Locate every blood parasite and identify its species.
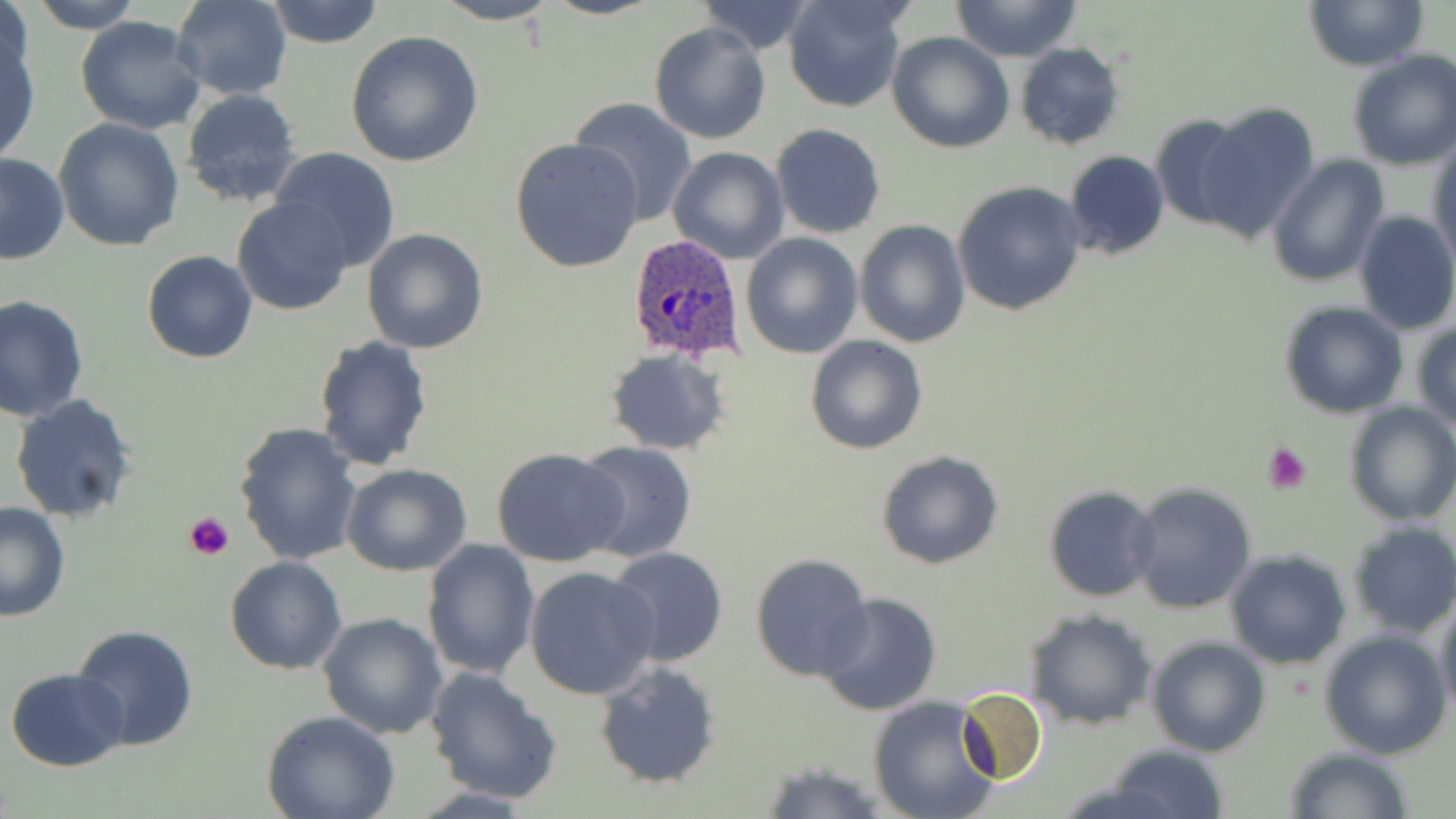

Approximate bounding boxes as named x1/y1/x2/y2 corners in pixels.
Plasmodium ovale-infected red blood cells: (x1=626, y1=234, x2=748, y2=361).
No Plasmodium falciparum, Plasmodium malariae, Plasmodium vivax, Babesia divergens, or Trypanosoma brucei observed.

Uninfected red blood cell locations: (x1=26, y1=0, x2=149, y2=32), (x1=171, y1=0, x2=290, y2=99), (x1=536, y1=0, x2=663, y2=19), (x1=783, y1=0, x2=912, y2=114), (x1=949, y1=0, x2=1082, y2=61), (x1=1303, y1=0, x2=1429, y2=70), (x1=2, y1=1, x2=34, y2=97), (x1=265, y1=1, x2=383, y2=48), (x1=433, y1=1, x2=560, y2=26), (x1=694, y1=1, x2=818, y2=55), (x1=75, y1=17, x2=207, y2=135), (x1=650, y1=22, x2=770, y2=144), (x1=1, y1=26, x2=39, y2=165), (x1=345, y1=30, x2=483, y2=166), (x1=887, y1=31, x2=1014, y2=152), (x1=1014, y1=42, x2=1125, y2=151), (x1=1346, y1=49, x2=1456, y2=170), (x1=180, y1=87, x2=303, y2=206), (x1=569, y1=97, x2=698, y2=226), (x1=1195, y1=101, x2=1322, y2=240), (x1=1150, y1=112, x2=1257, y2=231), (x1=54, y1=116, x2=184, y2=253), (x1=771, y1=123, x2=885, y2=239), (x1=510, y1=136, x2=644, y2=272), (x1=1429, y1=137, x2=1456, y2=270), (x1=667, y1=147, x2=789, y2=264), (x1=270, y1=148, x2=401, y2=274), (x1=1063, y1=149, x2=1169, y2=259), (x1=0, y1=153, x2=69, y2=265), (x1=1267, y1=153, x2=1389, y2=288), (x1=952, y1=180, x2=1087, y2=316), (x1=232, y1=196, x2=353, y2=316), (x1=1353, y1=210, x2=1456, y2=337), (x1=855, y1=220, x2=971, y2=348), (x1=361, y1=228, x2=488, y2=354), (x1=741, y1=232, x2=864, y2=358), (x1=142, y1=250, x2=259, y2=364), (x1=1, y1=296, x2=90, y2=425), (x1=1279, y1=301, x2=1409, y2=419), (x1=1411, y1=324, x2=1456, y2=434), (x1=314, y1=336, x2=434, y2=471), (x1=806, y1=336, x2=928, y2=455), (x1=605, y1=348, x2=730, y2=455), (x1=9, y1=393, x2=139, y2=523), (x1=1343, y1=402, x2=1456, y2=526), (x1=233, y1=420, x2=363, y2=565), (x1=575, y1=440, x2=698, y2=563), (x1=492, y1=449, x2=628, y2=568), (x1=877, y1=452, x2=1004, y2=570), (x1=342, y1=464, x2=473, y2=578), (x1=1126, y1=481, x2=1258, y2=616), (x1=1043, y1=484, x2=1160, y2=602), (x1=1, y1=502, x2=71, y2=621), (x1=1344, y1=522, x2=1456, y2=639), (x1=423, y1=539, x2=541, y2=680), (x1=604, y1=546, x2=730, y2=667), (x1=1224, y1=549, x2=1352, y2=668), (x1=749, y1=552, x2=875, y2=680), (x1=225, y1=556, x2=348, y2=674), (x1=524, y1=566, x2=662, y2=700), (x1=814, y1=592, x2=942, y2=716), (x1=1434, y1=599, x2=1456, y2=720), (x1=1027, y1=610, x2=1156, y2=731), (x1=319, y1=611, x2=447, y2=739), (x1=71, y1=625, x2=198, y2=751), (x1=1318, y1=628, x2=1452, y2=759), (x1=1146, y1=635, x2=1270, y2=755), (x1=594, y1=661, x2=722, y2=788), (x1=6, y1=667, x2=129, y2=771), (x1=425, y1=667, x2=561, y2=804), (x1=954, y1=687, x2=1048, y2=785), (x1=868, y1=696, x2=1002, y2=819), (x1=262, y1=711, x2=402, y2=819), (x1=1107, y1=744, x2=1231, y2=819), (x1=1282, y1=747, x2=1414, y2=819), (x1=755, y1=758, x2=887, y2=817). Platelet locations: (x1=1263, y1=442, x2=1312, y2=493), (x1=184, y1=510, x2=235, y2=559). Slide-level diagnosis: Plasmodium ovale. Thin blood smear. Optical microscopy. Image is 1456×819 pixels. One field of a larger specimen. Captured at 1000x magnification. May-Grünwald-Giemsa stain.